Identify the preparation type.
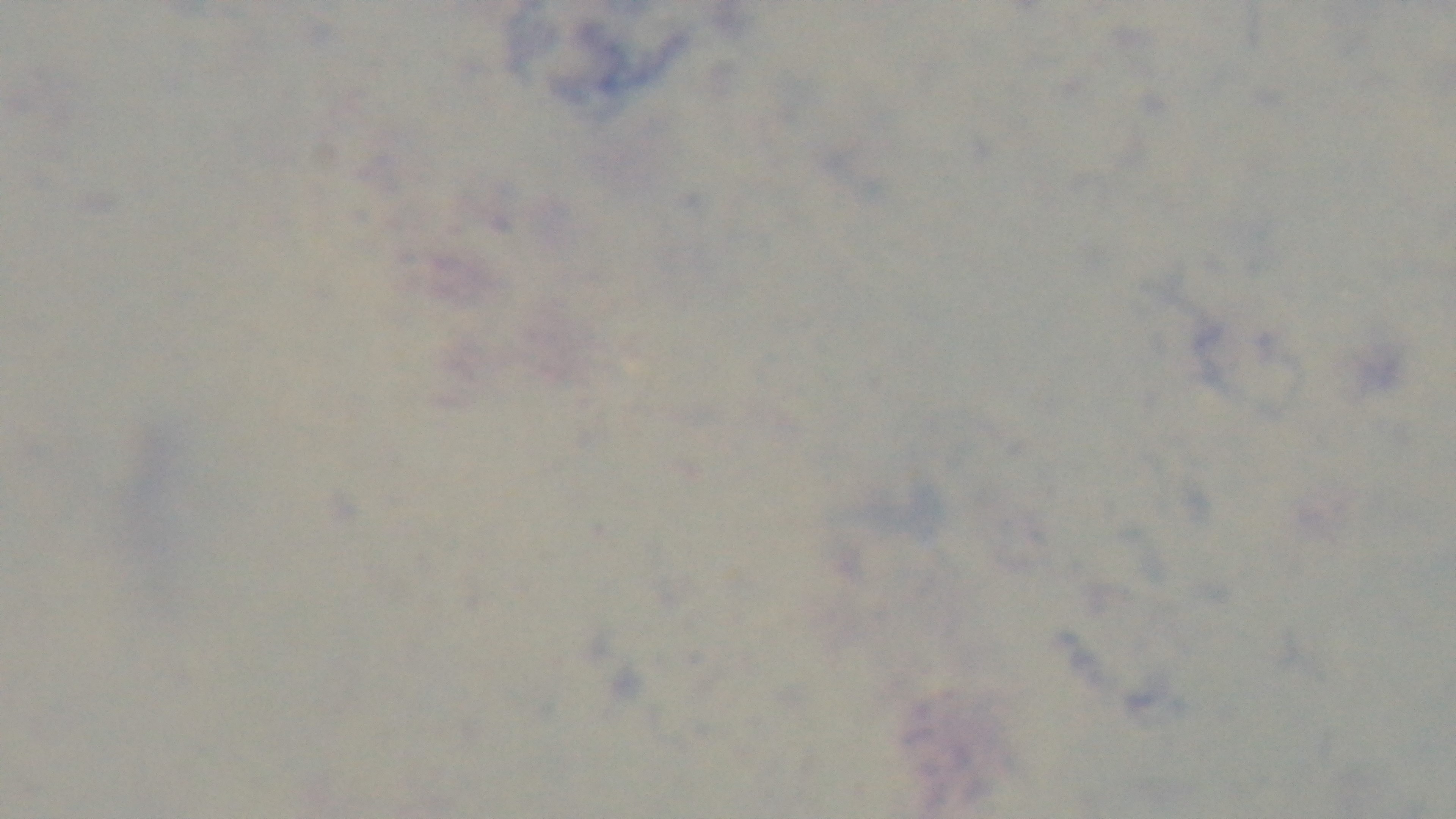

A thick smear.

stain: Giemsa
field_of_view: one from the slide
malaria_status: uninfected
capture: mounted 4K digital camera
modality: light microscopy
objective: 100x oil immersion